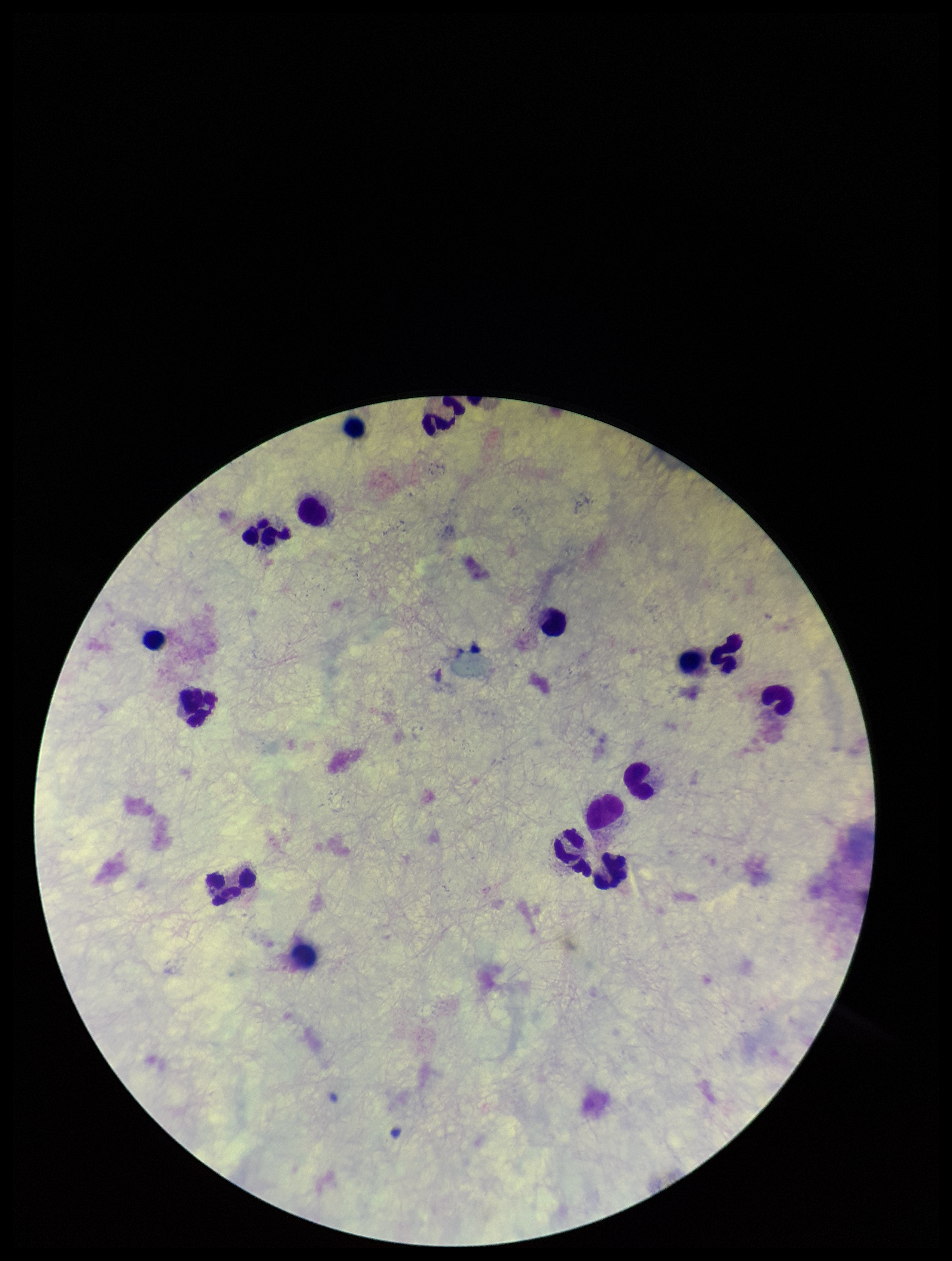

preparation = thick smear
parasite count = 0
field of view = one from this slide
image size = 952×1261 pixels
capture = smartphone photograph through the microscope eyepiece
patient malaria status = negative
leukocyte count = 15
stain = Giemsa
Plasmodium parasites = none identified